Locate every blood parasite and identify its species.
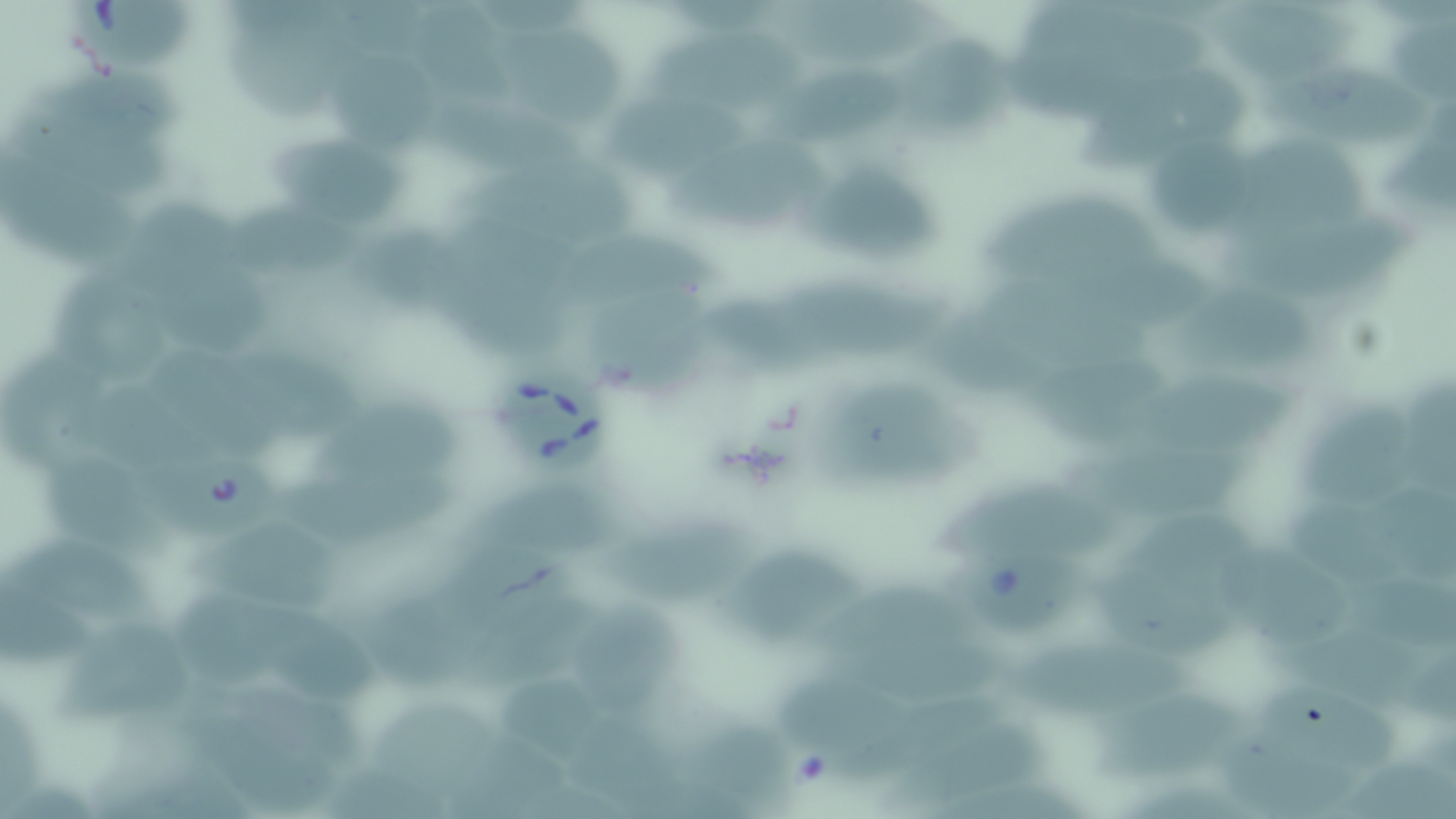

Approximate bounding boxes as [x1, y1, x2, y2] in pixels.
Babesia divergens-infected red blood cells: [63, 0, 208, 78], [499, 368, 617, 473], [149, 458, 276, 537], [959, 552, 1086, 633].
No Plasmodium falciparum, Plasmodium ovale, Plasmodium malariae, Plasmodium vivax, or Trypanosoma brucei observed.

slide-level diagnosis = Babesia divergens
stain = May-Grünwald-Giemsa
magnification = 1000x
field of view = single
uninfected red blood cell locations = approximate bounding boxes as [x1, y1, x2, y2] in pixels: [410, 0, 519, 115], [1213, 0, 1350, 90], [1027, 2, 1219, 96], [788, 5, 945, 58], [1397, 18, 1453, 111], [233, 19, 369, 132], [504, 37, 630, 135], [649, 37, 820, 115], [902, 42, 1011, 128], [1014, 42, 1160, 116], [747, 50, 902, 152], [46, 59, 185, 145], [1274, 61, 1424, 135], [346, 68, 448, 152], [1067, 69, 1241, 178], [16, 101, 180, 199], [610, 101, 755, 182], [422, 104, 584, 184], [1397, 113, 1456, 218], [1247, 131, 1382, 223], [1161, 136, 1259, 226], [277, 141, 409, 212], [672, 143, 846, 239], [5, 149, 139, 273], [472, 155, 646, 253], [819, 165, 953, 274], [1000, 186, 1170, 273], [129, 195, 248, 293], [237, 202, 375, 279], [1243, 215, 1405, 290], [575, 234, 719, 308], [382, 236, 491, 329], [458, 240, 582, 360], [1058, 253, 1227, 308], [168, 259, 281, 371], [59, 263, 189, 400], [796, 275, 946, 349], [988, 279, 1165, 380], [1192, 282, 1329, 361], [584, 295, 721, 399], [727, 301, 842, 383], [941, 305, 1058, 383], [8, 348, 121, 482], [247, 352, 366, 442], [165, 353, 287, 458], [1046, 360, 1169, 431], [1146, 364, 1310, 444], [837, 375, 975, 493], [86, 380, 231, 482], [1404, 384, 1456, 491], [331, 392, 465, 481], [1304, 395, 1392, 497], [1081, 430, 1271, 505], [52, 450, 184, 565], [302, 458, 464, 538], [946, 481, 1121, 550], [473, 482, 618, 544], [1371, 483, 1456, 588], [1290, 497, 1408, 585], [1146, 501, 1288, 577], [605, 523, 753, 607], [205, 526, 349, 613], [464, 538, 570, 623], [25, 541, 159, 623], [1233, 547, 1343, 651], [724, 550, 861, 631], [1099, 556, 1251, 645], [1345, 564, 1445, 652], [1, 565, 92, 671], [814, 586, 980, 643], [462, 589, 605, 678], [193, 593, 315, 687], [378, 593, 469, 682], [570, 597, 689, 703], [284, 619, 391, 700], [1290, 621, 1421, 698], [68, 623, 197, 725], [828, 631, 1008, 684], [1012, 635, 1189, 698], [1402, 660, 1456, 726], [496, 670, 587, 754], [774, 674, 918, 749], [252, 686, 359, 773], [1256, 686, 1396, 755], [1074, 694, 1255, 777], [3, 695, 50, 817], [377, 696, 507, 788], [851, 696, 1003, 772], [193, 702, 338, 817], [685, 704, 799, 814], [574, 707, 682, 810], [894, 727, 1051, 804], [1223, 730, 1365, 813], [468, 731, 558, 808], [1349, 745, 1444, 817], [332, 755, 458, 819]
image size = 1456×819 pixels
preparation = thin blood film
modality = optical microscopy